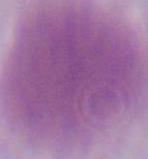
A red blood cell is seen. Photomicrograph. Captured at 1000x magnification.